Name the parasite shown.
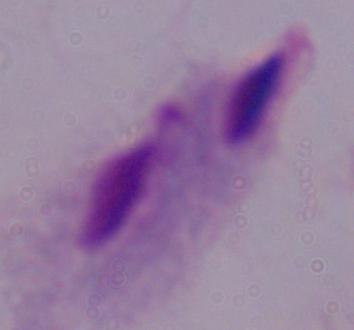

This is a trichomonad.

Summary:
  - Modality: photomicrograph
  - Magnification: 1000x